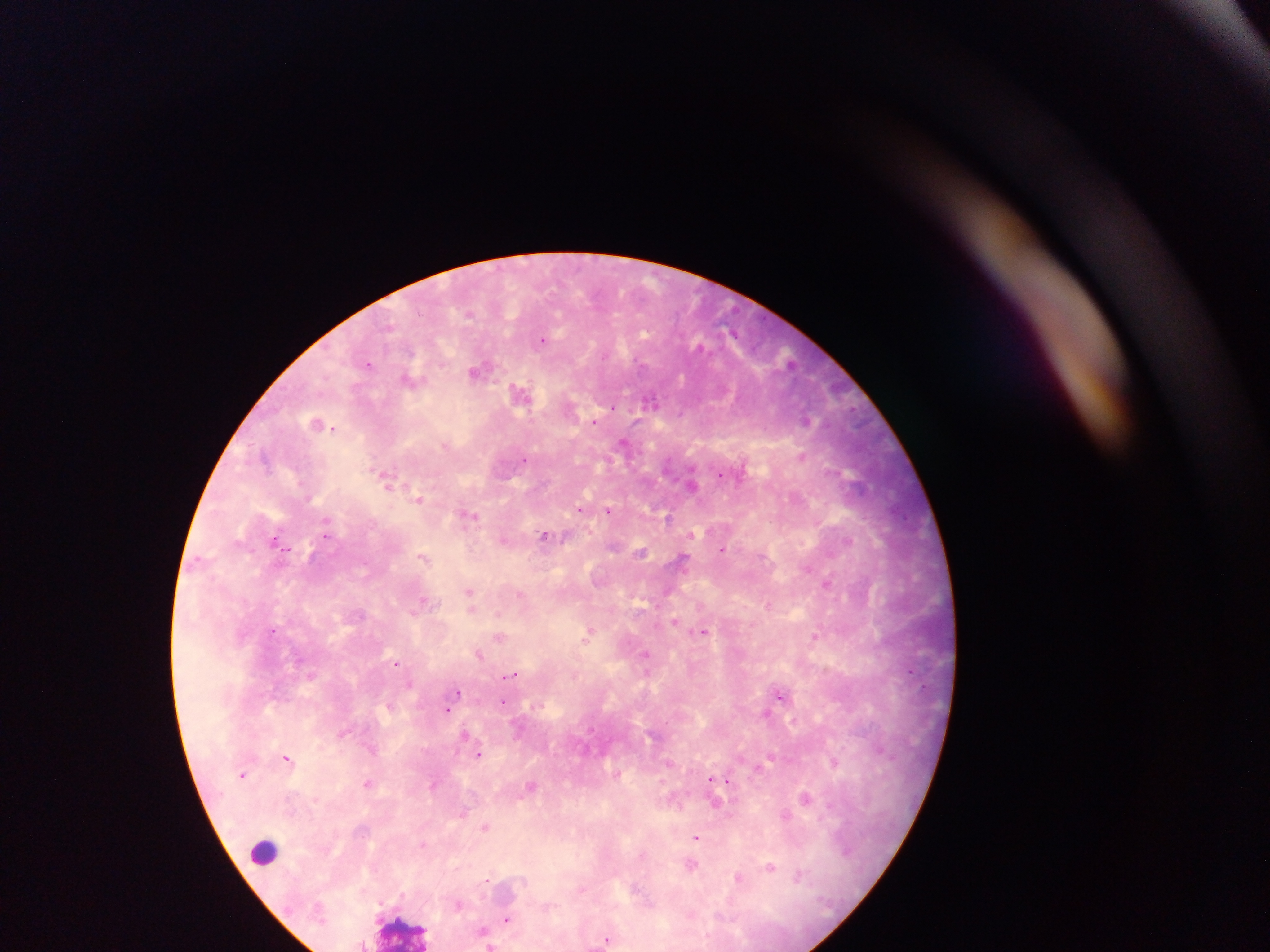
Approximate centers as x y in pixels.
Summary:
  - Malaria parasite locations: 470 315; 645 333; 544 340; 790 361; 368 362; 478 370; 520 390; 649 399; 613 407; 594 420; 624 440; 802 454; 525 461; 385 472; 849 473; 695 485; 390 488; 419 499; 582 508; 608 511; 469 516; 668 517; 326 520; 545 536; 273 538; 848 543; 724 549; 288 550; 311 555; 423 558; 683 558; 828 581; 469 591; 521 594; 422 601; 768 605; 471 607; 414 610; 498 614; 362 615; 675 621; 272 629; 703 630; 587 633; 500 636; 816 636; 644 652; 480 655; 396 662; 510 674; 458 691; 782 695; 502 702; 448 710; 767 713; 465 733; 881 749; 480 753; 287 758; 772 759; 834 763; 242 773; 711 780; 369 783; 432 785; 806 798; 462 813; 785 815; 486 828; 695 836; 422 846; 771 866; 800 874; 738 876; 524 882; 581 890; 457 904; 551 907; 505 917; 481 928; 606 941; 491 944
  - Leukocyte locations: 254 854; 399 928
  - Country: Ghana
  - Capture: mobile-phone photograph through a microscope
  - Preparation: thick blood smear
  - Image size: 1270×952 pixels
  - Field of view: single